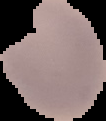
From a thin blood film. Image is 106×121 pixels. The area outside the segmented cell region is set to black. Malaria status: parasitized.